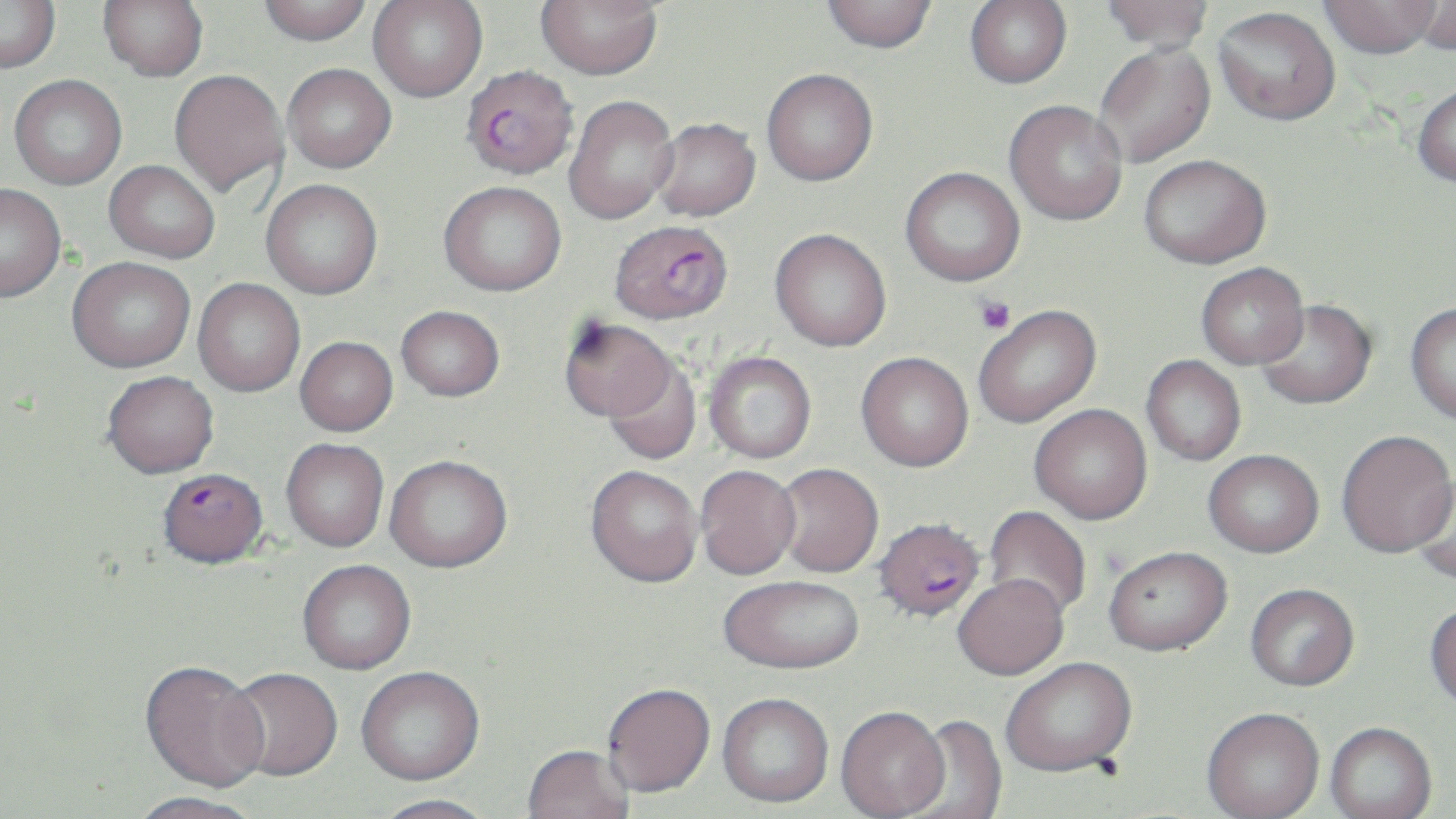
Summary:
  - Coordinate format: approximate bounding boxes as (x1,y1)-(x2,y2) corner pairs in pixels
  - Platelet locations: (974,296)-(1015,334)
  - Uninfected red blood cell locations: (0,0)-(61,73), (99,0)-(208,80), (257,0)-(372,44), (368,0)-(487,101), (535,0)-(662,80), (820,0)-(938,53), (965,0)-(1072,88), (1100,0)-(1214,54), (1411,0)-(1456,57), (1320,1)-(1441,59), (1214,7)-(1341,126), (1094,42)-(1215,167), (282,63)-(396,173), (761,68)-(878,185), (169,70)-(288,196), (9,74)-(127,189), (1412,82)-(1456,187), (565,95)-(678,224), (1003,100)-(1128,226), (650,118)-(761,221), (1139,154)-(1271,268), (104,160)-(220,263), (900,166)-(1025,287), (261,179)-(383,300), (439,180)-(567,296), (0,183)-(66,302), (770,228)-(892,351), (67,256)-(196,372), (1196,263)-(1308,369), (193,278)-(305,397), (1255,299)-(1377,409), (1405,302)-(1456,425), (396,305)-(504,401), (973,305)-(1101,428), (559,317)-(676,423), (295,336)-(398,436), (704,351)-(816,463), (856,352)-(974,471), (1141,355)-(1246,465), (603,359)-(701,465), (102,370)-(219,478), (1029,404)-(1152,524), (1336,430)-(1455,557), (281,438)-(389,552), (1203,449)-(1324,557), (384,454)-(513,573), (773,463)-(883,578), (585,465)-(702,589), (695,465)-(802,580), (1410,471)-(1456,586), (984,505)-(1092,620), (1104,545)-(1232,656), (297,560)-(417,674), (953,574)-(1069,680), (718,576)-(865,676), (1245,583)-(1359,691), (1425,600)-(1456,711), (1001,657)-(1137,777), (140,662)-(270,794), (356,668)-(484,788), (225,669)-(343,783), (602,685)-(716,800), (716,695)-(833,810), (836,707)-(951,818), (1202,707)-(1324,818), (901,715)-(1008,819), (1325,722)-(1437,819), (522,746)-(633,819), (128,793)-(264,819), (372,795)-(497,819)
  - Plasmodium falciparum-infected red blood cell locations: (461,66)-(578,180), (609,219)-(733,324), (158,467)-(267,568), (872,517)-(986,622)
  - Slide-level diagnosis: Plasmodium falciparum
  - Magnification: 1000x
  - Image size: 1456×819 pixels
  - Stain: May-Grünwald-Giemsa
  - Field of view: one of a larger specimen
  - Preparation: thin blood smear
  - Modality: optical microscopy